Assess the morphology of the erythrocytes.
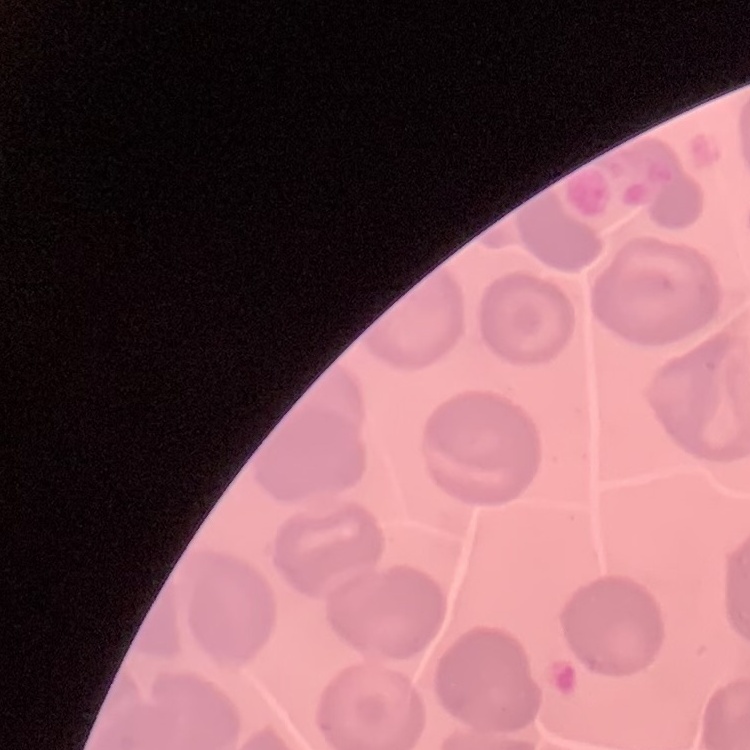

They show no rouleaux formation.

Field's or Giemsa stain. Square crop of a larger photomicrograph. Thin blood smear.